Identify the parasite.
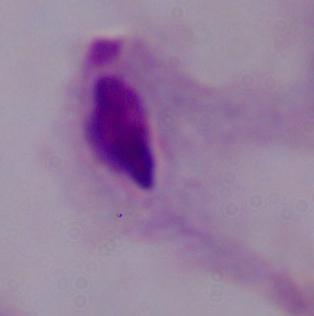
This is a trichomonad.

Captured at 1000x magnification. Micrograph.